Assess the morphology of the erythrocytes.
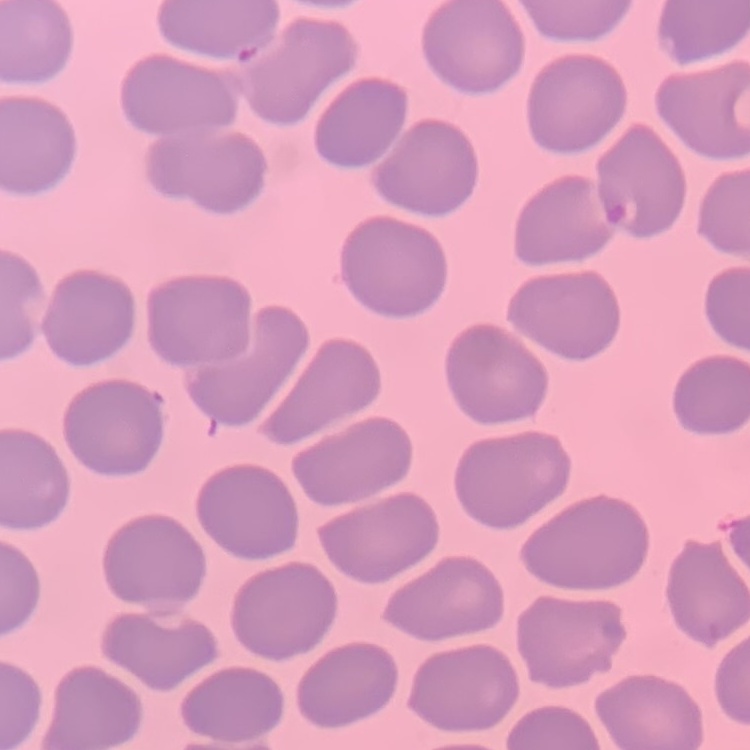
They show no rouleaux formation.

Stained with either Field's or Giemsa. One tile cut from a larger photomicrograph. Thin blood film.